Locate every Plasmodium parasite.
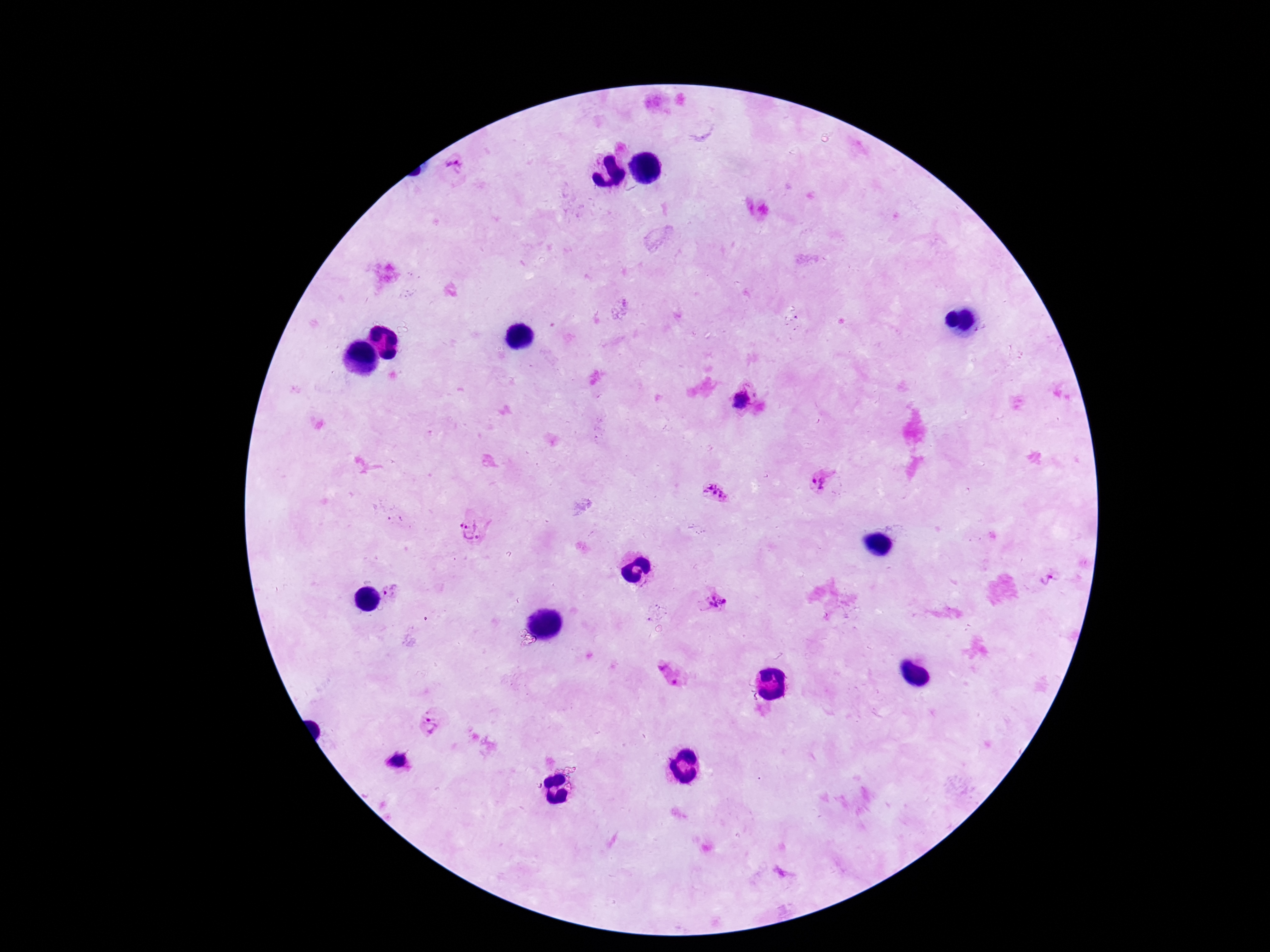

Approximate centers as (x, y) in pixels.
Plasmodium parasites: (455, 163), (742, 401), (818, 481), (716, 493), (474, 529), (1048, 578), (389, 591), (714, 602), (669, 673), (431, 724), (399, 761).

Summary:
  - Magnification: 100x
  - Patient malaria status: positive
  - Stain: Giemsa
  - Capture: smartphone camera through the microscope eyepiece
  - Preparation: thick blood smear
  - Image size: 1270×952 pixels
  - Field of view: one from this slide